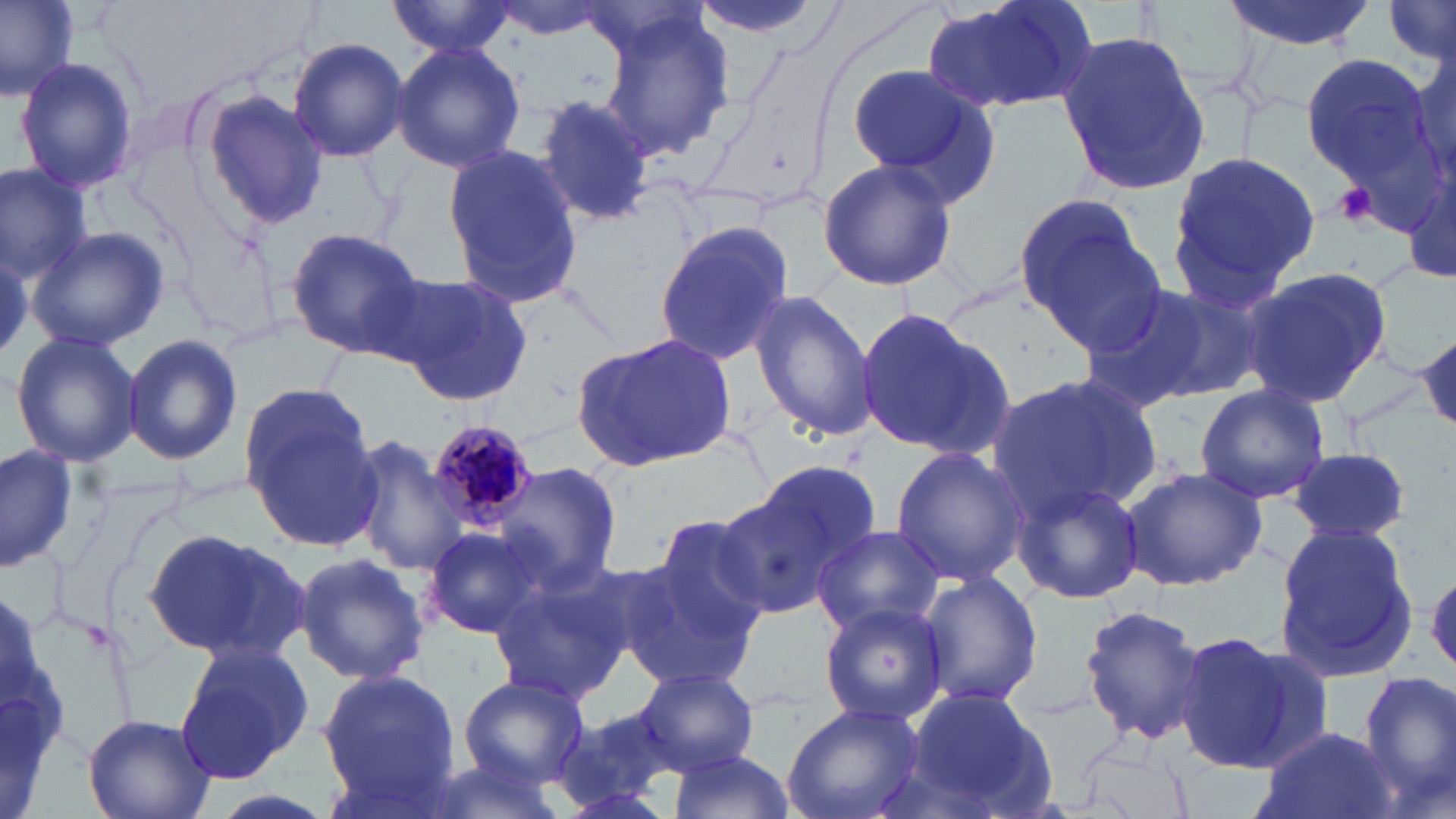

slide_level_diagnosis: Plasmodium malariae
modality: optical microscopy
magnification: 1000x
platelet_locations: 'approximate bounding boxes as named x1/y1/x2/y2 corners in pixels: (x1=1329, y1=181, x2=1381, y2=229)'
field_of_view: one of a larger specimen
uninfected_red_blood_cell_locations: 'approximate bounding boxes as named x1/y1/x2/y2 corners in pixels: (x1=0, y1=0, x2=80, y2=103), (x1=684, y1=0, x2=830, y2=40), (x1=920, y1=0, x2=1101, y2=117), (x1=1224, y1=0, x2=1375, y2=52), (x1=388, y1=1, x2=518, y2=57), (x1=1380, y1=1, x2=1456, y2=73), (x1=491, y1=2, x2=617, y2=39), (x1=596, y1=9, x2=736, y2=164), (x1=1055, y1=29, x2=1213, y2=199), (x1=1408, y1=33, x2=1454, y2=190), (x1=288, y1=38, x2=409, y2=162), (x1=392, y1=41, x2=527, y2=173), (x1=1300, y1=53, x2=1433, y2=186), (x1=13, y1=55, x2=141, y2=196), (x1=846, y1=60, x2=1004, y2=199), (x1=201, y1=93, x2=329, y2=228), (x1=534, y1=93, x2=655, y2=224), (x1=440, y1=145, x2=586, y2=311), (x1=1165, y1=147, x2=1320, y2=307), (x1=1405, y1=155, x2=1455, y2=292), (x1=815, y1=159, x2=958, y2=290), (x1=0, y1=163, x2=92, y2=282), (x1=1012, y1=192, x2=1163, y2=348), (x1=654, y1=221, x2=799, y2=370), (x1=25, y1=227, x2=169, y2=353), (x1=284, y1=227, x2=428, y2=359), (x1=1239, y1=265, x2=1395, y2=408), (x1=393, y1=272, x2=535, y2=406), (x1=1084, y1=281, x2=1263, y2=409), (x1=748, y1=290, x2=879, y2=443), (x1=854, y1=307, x2=1012, y2=462), (x1=575, y1=332, x2=739, y2=471), (x1=1411, y1=332, x2=1455, y2=435), (x1=122, y1=333, x2=243, y2=464), (x1=11, y1=334, x2=142, y2=467), (x1=987, y1=371, x2=1161, y2=518), (x1=241, y1=384, x2=378, y2=546), (x1=1193, y1=384, x2=1330, y2=505), (x1=348, y1=434, x2=470, y2=578), (x1=0, y1=445, x2=79, y2=572), (x1=888, y1=446, x2=1030, y2=586), (x1=1288, y1=448, x2=1412, y2=546), (x1=493, y1=463, x2=621, y2=593), (x1=1120, y1=465, x2=1267, y2=592), (x1=720, y1=472, x2=869, y2=619), (x1=1010, y1=474, x2=1149, y2=605), (x1=643, y1=509, x2=779, y2=653), (x1=1271, y1=518, x2=1421, y2=682), (x1=812, y1=524, x2=945, y2=637), (x1=421, y1=526, x2=548, y2=641), (x1=144, y1=529, x2=309, y2=662), (x1=613, y1=549, x2=760, y2=689), (x1=293, y1=551, x2=432, y2=684), (x1=913, y1=569, x2=1043, y2=709), (x1=485, y1=573, x2=629, y2=704), (x1=819, y1=603, x2=949, y2=724), (x1=1078, y1=604, x2=1209, y2=744), (x1=1171, y1=629, x2=1301, y2=772), (x1=174, y1=640, x2=313, y2=783), (x1=633, y1=666, x2=760, y2=776), (x1=318, y1=668, x2=461, y2=798), (x1=1358, y1=672, x2=1456, y2=814), (x1=458, y1=675, x2=590, y2=786), (x1=901, y1=686, x2=1059, y2=818), (x1=783, y1=702, x2=925, y2=819), (x1=550, y1=705, x2=693, y2=816), (x1=83, y1=716, x2=216, y2=819), (x1=1252, y1=724, x2=1398, y2=819), (x1=666, y1=750, x2=795, y2=819), (x1=418, y1=755, x2=571, y2=819)'
image_size: 1456×819 pixels
stain: May-Grünwald-Giemsa
plasmodium_malariae_infected_red_blood_cell_locations: 'approximate bounding boxes as named x1/y1/x2/y2 corners in pixels: (x1=427, y1=415, x2=541, y2=529)'
preparation: thin blood smear
white_blood_cell_locations: 'approximate bounding boxes as named x1/y1/x2/y2 corners in pixels: (x1=1, y1=570, x2=78, y2=819)'